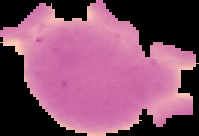
Summary:
  - Image type: segmented cell region on a black background
  - Result: no malaria parasites seen
  - Image size: 199×136 pixels
  - Preparation: thin blood film